Assess the morphology of the red blood cells.
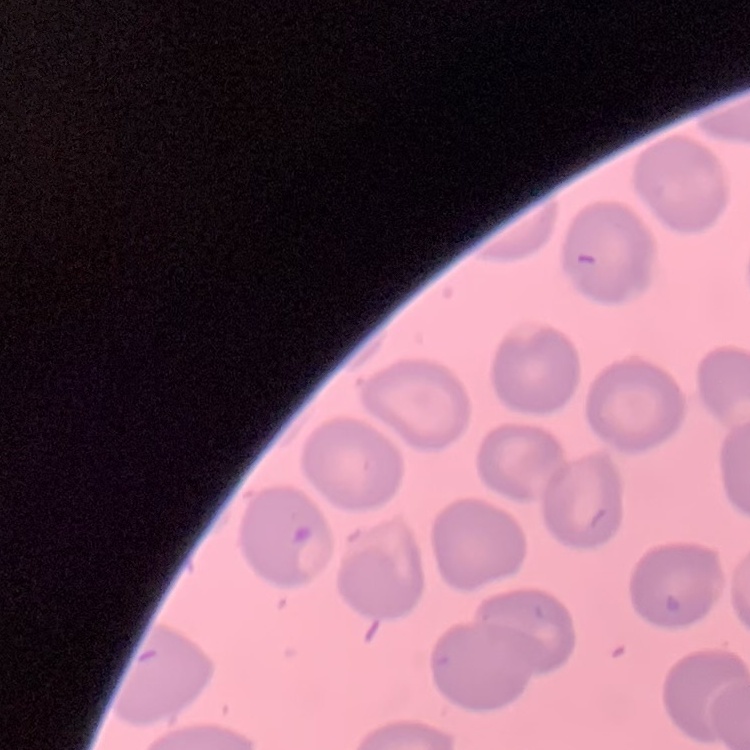
No rouleaux formation.

Summary:
  - Image type: square crop of a larger photomicrograph
  - Preparation: thin blood smear
  - Stain: Field's or Giemsa